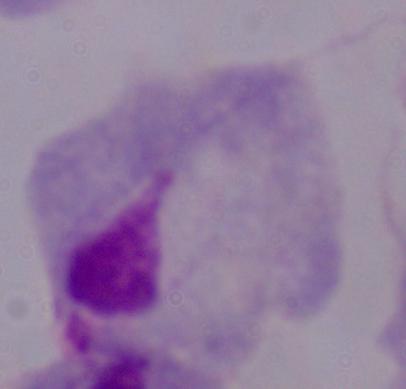 Captured at 1000x magnification. A trichomonad is seen. Micrograph.